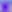

{
  "identification": "Toxoplasma gondii",
  "magnification": "400x",
  "modality": "micrograph"
}